State which parasite is depicted.
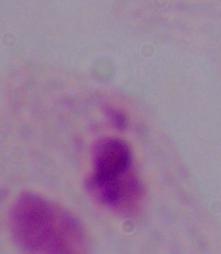
A trichomonad.

{
  "magnification": "1000x",
  "modality": "micrograph"
}